State the blood parasite species.
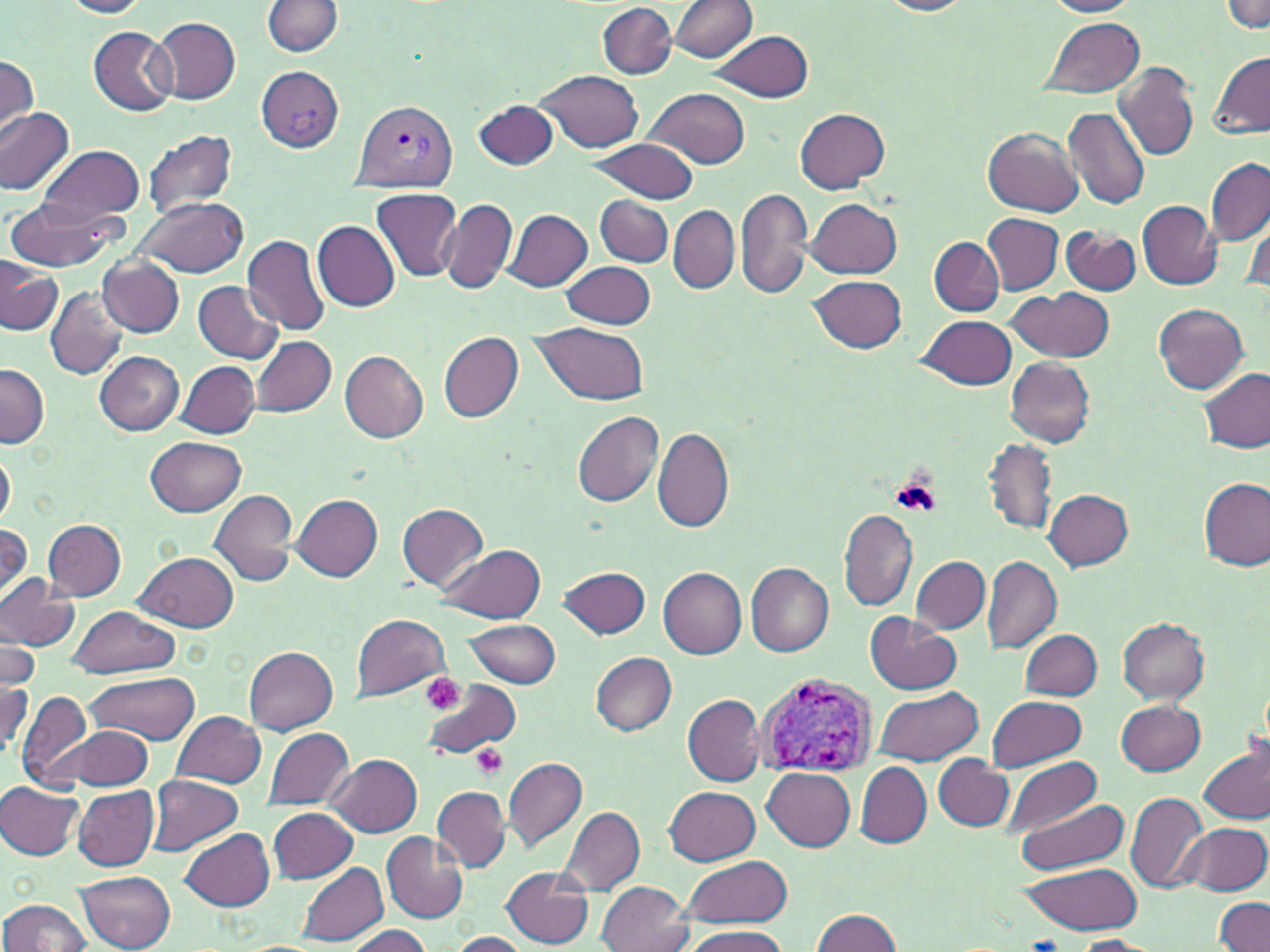
Plasmodium vivax.

magnification = 1000x
platelet locations = approximate bounding boxes as (x1, y1, x2, y2) in pixels: (890, 473, 940, 518), (418, 674, 466, 716), (470, 743, 507, 779)
Plasmodium vivax-infected red blood cell locations = approximate bounding boxes as (x1, y1, x2, y2) in pixels: (352, 100, 459, 194), (758, 673, 879, 777)
modality = optical microscopy
stain = May-Grünwald-Giemsa
field of view = single
image size = 1270×952 pixels
preparation = thin blood smear
uninfected red blood cell locations = approximate bounding boxes as (x1, y1, x2, y2) in pixels: (60, 0, 153, 18), (877, 0, 976, 16), (1042, 0, 1141, 17), (264, 1, 343, 56), (1222, 1, 1269, 33), (672, 2, 757, 62), (598, 3, 677, 79), (1038, 16, 1146, 98), (153, 17, 240, 103), (89, 26, 178, 114), (707, 30, 815, 103), (1208, 51, 1270, 137), (0, 54, 38, 140), (1112, 61, 1198, 162), (537, 70, 642, 151), (645, 88, 751, 168), (475, 98, 557, 169), (1062, 106, 1151, 211), (0, 108, 75, 195), (795, 108, 891, 193), (984, 127, 1083, 217), (145, 130, 238, 216), (587, 139, 699, 203), (38, 144, 146, 223), (1206, 157, 1270, 245), (371, 188, 463, 279), (736, 189, 813, 300), (596, 195, 674, 266), (135, 196, 248, 277), (5, 197, 122, 272), (806, 197, 902, 277), (438, 198, 516, 295), (1138, 201, 1222, 290), (669, 205, 739, 294), (504, 209, 592, 290), (1243, 213, 1268, 293), (983, 215, 1063, 293), (313, 220, 400, 311), (1060, 225, 1141, 297), (242, 233, 331, 338), (929, 237, 1004, 317), (98, 255, 183, 337), (0, 257, 62, 335), (563, 261, 656, 328), (808, 274, 906, 354), (195, 280, 285, 363), (46, 287, 128, 379), (1010, 288, 1114, 363), (1154, 305, 1248, 394), (919, 314, 1017, 390), (533, 322, 649, 405), (438, 332, 524, 423), (251, 336, 336, 416), (339, 350, 429, 441), (94, 351, 183, 434), (1006, 358, 1095, 447), (178, 362, 260, 438), (1, 363, 48, 447), (1199, 367, 1269, 453), (573, 411, 663, 507), (653, 427, 733, 533), (146, 436, 247, 516), (983, 440, 1057, 532), (0, 447, 17, 525), (1199, 478, 1269, 570), (208, 489, 298, 587), (1044, 489, 1133, 570), (292, 494, 383, 581), (396, 503, 488, 590), (839, 510, 917, 611), (44, 519, 126, 601), (0, 523, 32, 603), (438, 543, 546, 623), (135, 550, 239, 633), (909, 556, 990, 632), (981, 556, 1061, 656), (747, 562, 834, 657), (560, 566, 651, 639), (659, 567, 748, 659), (0, 572, 80, 652), (65, 606, 181, 677), (352, 614, 449, 701), (866, 615, 961, 693), (1118, 618, 1210, 704), (464, 619, 562, 687), (2, 626, 39, 691), (1020, 628, 1101, 699), (245, 647, 337, 735), (590, 652, 676, 735), (85, 673, 200, 744), (420, 677, 522, 761), (0, 678, 33, 759), (873, 686, 983, 766), (17, 691, 92, 790), (683, 693, 765, 787), (988, 695, 1088, 771), (1117, 700, 1207, 775), (172, 710, 266, 789), (263, 726, 355, 808), (71, 727, 153, 789), (1198, 745, 1270, 824), (501, 754, 589, 854), (933, 754, 1013, 831), (327, 755, 422, 836), (1003, 757, 1101, 838), (855, 761, 931, 848), (762, 768, 856, 851), (144, 775, 241, 857), (1, 781, 86, 860), (157, 783, 260, 906), (74, 786, 158, 871), (432, 786, 510, 872), (664, 786, 760, 865), (1125, 792, 1208, 893), (1011, 796, 1132, 874), (554, 805, 646, 898), (268, 808, 356, 883), (1183, 821, 1268, 894), (181, 828, 277, 913), (382, 833, 469, 923), (679, 857, 793, 927), (298, 861, 389, 945), (1018, 862, 1144, 934), (501, 867, 595, 947), (76, 869, 175, 952), (594, 882, 694, 951), (0, 897, 93, 951), (1216, 898, 1270, 952), (810, 909, 903, 952), (345, 925, 434, 952), (684, 926, 791, 952), (447, 931, 530, 951), (1071, 936, 1160, 951)